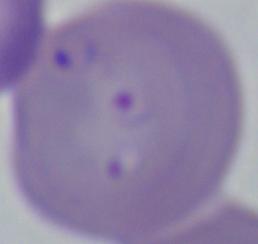
identification = Babesia
magnification = 1000x
modality = micrograph